Assess this cell for malaria.
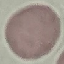

It is uninfected.

Giemsa-stained preparation. Thin blood film. Acquired by smartphone through the microscope eyepiece. Automatically extracted cell patch, resized to 64 × 64 pixels.